Name the parasite shown.
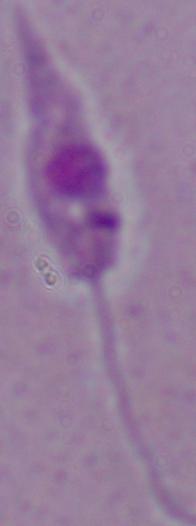
Leishmania.

Photomicrograph. 1000x magnification.